Locate every leukocyte (white blood cell).
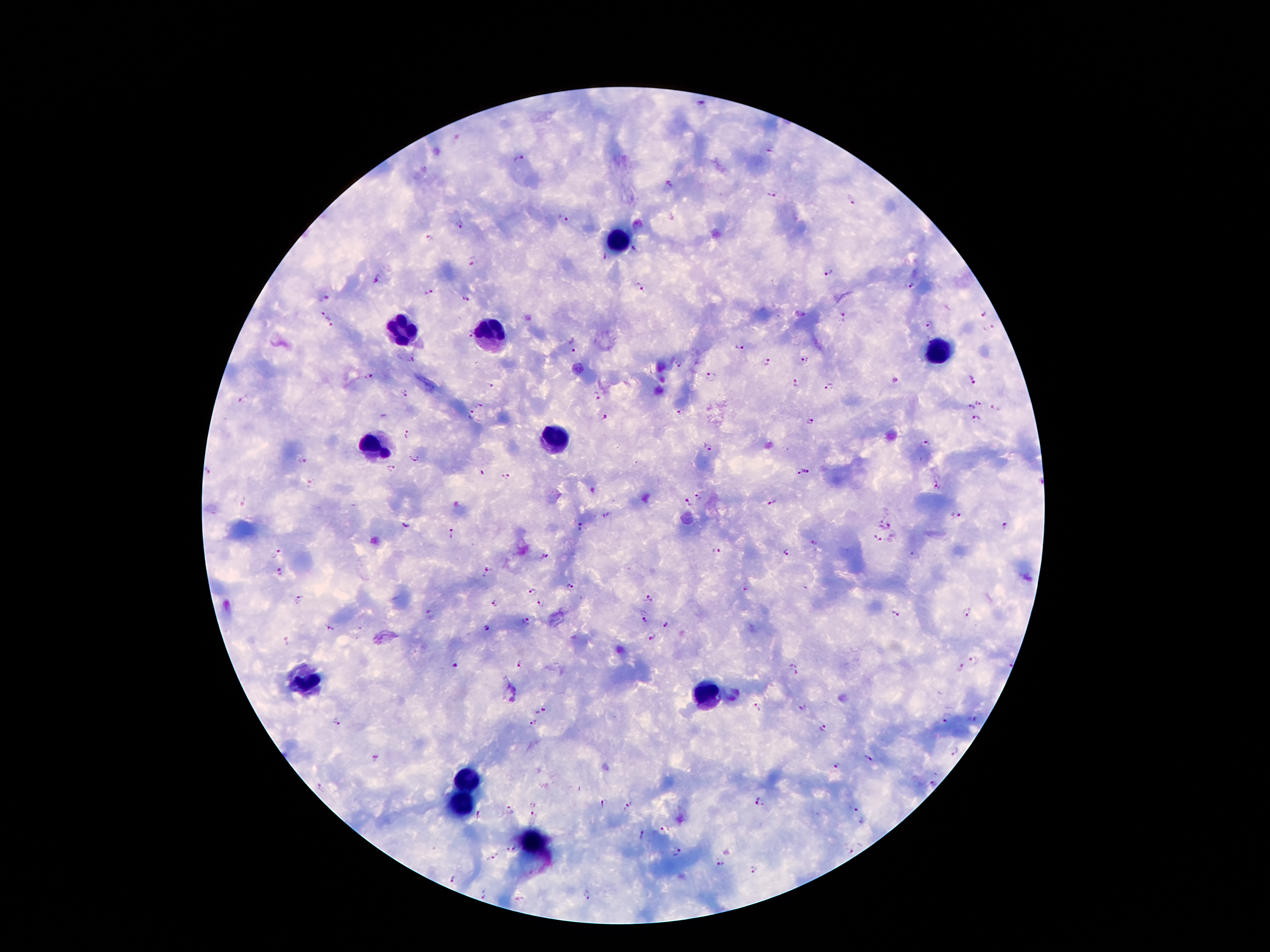

Approximate centers as (x, y) in pixels.
Leukocytes: (618, 241), (402, 331), (484, 336), (941, 352), (555, 438), (371, 443), (303, 680), (707, 693), (465, 779), (460, 805), (534, 845).

Plasmodium parasite locations: (699, 103), (771, 150), (521, 159), (669, 184), (771, 194), (850, 199), (563, 218), (458, 226), (427, 238), (634, 251), (604, 257), (474, 262), (829, 271), (375, 280), (911, 287), (640, 288), (426, 292), (325, 297), (466, 298), (324, 314), (985, 315), (845, 318), (330, 325), (927, 325), (989, 329), (574, 344), (738, 346), (413, 358), (805, 359), (679, 362), (767, 362), (711, 375), (369, 376), (972, 379), (896, 381), (795, 382), (492, 385), (830, 387), (404, 394), (598, 395), (244, 400), (979, 401), (480, 404), (970, 407), (995, 408), (681, 411), (471, 416), (605, 419), (975, 419), (811, 423), (409, 435), (925, 442), (706, 445), (414, 457), (303, 460), (391, 470), (796, 471), (809, 471), (208, 473), (481, 473), (506, 476), (311, 482), (937, 488), (699, 494), (244, 502), (771, 502), (687, 503), (607, 515), (956, 515), (889, 524), (405, 525), (1004, 525), (581, 527), (451, 532), (876, 539), (815, 543), (716, 551), (785, 553), (275, 554), (913, 555), (544, 557), (487, 571), (279, 573), (571, 588), (744, 589), (531, 592), (301, 598), (649, 598), (494, 603), (542, 604), (967, 613), (430, 615), (896, 615), (643, 621), (525, 622), (665, 626), (329, 627), (486, 627), (653, 638), (288, 642), (973, 659), (518, 663), (455, 665), (961, 667), (796, 668), (802, 707), (756, 708), (541, 709), (946, 718), (974, 720), (335, 722), (533, 724), (822, 728), (955, 752), (375, 758), (869, 760), (836, 766), (932, 784), (321, 789), (603, 801), (761, 802), (534, 803), (628, 807), (853, 811), (509, 812), (478, 815), (534, 816), (665, 828), (642, 834), (512, 848), (849, 852), (678, 853), (493, 856), (720, 864), (752, 871), (451, 878), (483, 893), (587, 895). Image is 1270×952 pixels. One field from this slide. Thick peripheral-blood smear. 100x magnification. Patient malaria status: positive for Plasmodium falciparum. Giemsa stain. Photographed through the microscope eyepiece with a smartphone camera.